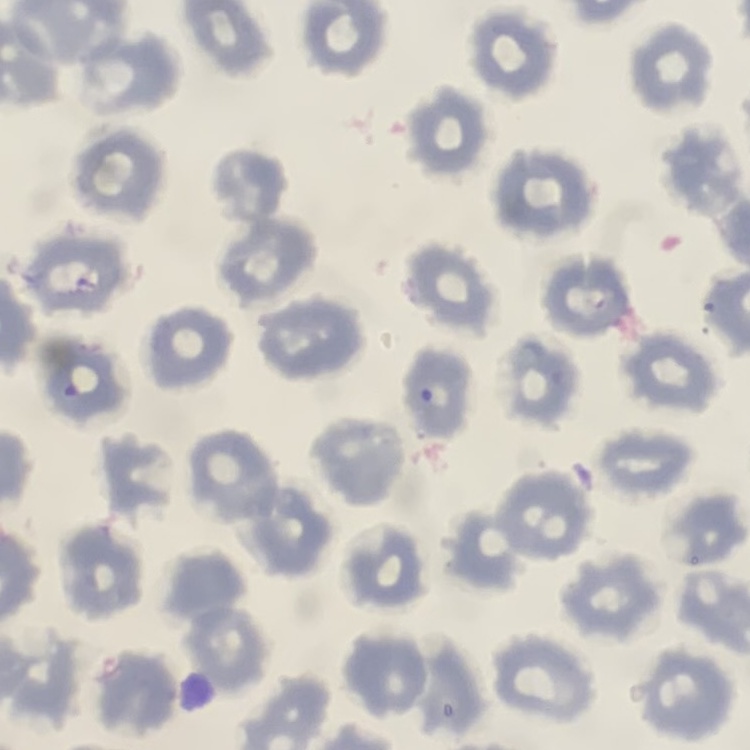
The erythrocytes show no rouleaux formation. One tile cut from a larger photomicrograph. Stained with either Field's or Giemsa. Thin peripheral smear.